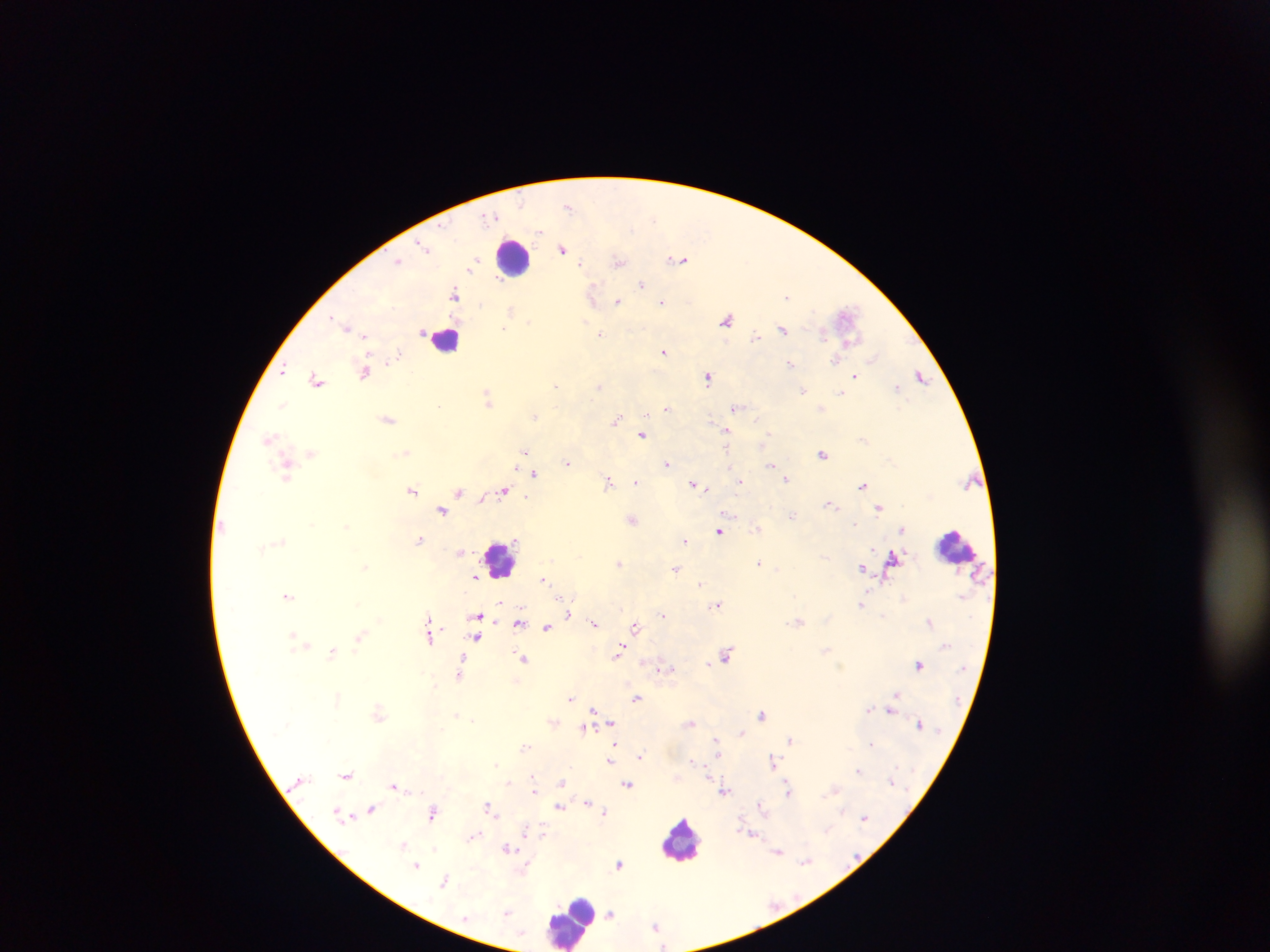 Approximate centers as (x, y) in pixels. Leukocyte locations: (514, 257), (446, 339), (957, 546), (500, 560), (680, 839), (609, 911), (570, 921). Malaria parasite locations: (568, 205), (422, 246), (563, 249), (681, 259), (399, 260), (618, 261), (473, 264), (471, 268), (641, 284), (454, 294), (788, 296), (593, 297), (662, 301), (618, 302), (512, 310), (848, 316), (726, 319), (530, 321), (347, 328), (505, 329), (783, 329), (822, 332), (602, 333), (757, 336), (849, 342), (664, 351), (399, 352), (836, 360), (791, 364), (282, 370), (365, 371), (710, 376), (854, 376), (921, 377), (317, 379), (556, 385), (600, 385), (898, 386), (803, 391), (488, 396), (737, 407), (821, 407), (667, 408), (535, 415), (388, 419), (617, 421), (727, 430), (642, 434), (269, 439), (863, 439), (525, 451), (726, 451), (407, 452), (311, 453), (823, 453), (567, 462), (668, 463), (771, 464), (286, 467), (535, 472), (286, 475), (786, 478), (608, 481), (637, 481), (740, 481), (863, 484), (696, 485), (412, 489), (504, 489), (459, 491), (481, 498), (832, 505), (879, 507), (443, 509), (792, 516), (633, 519), (346, 526), (757, 528), (904, 529), (720, 530), (419, 539), (686, 540), (462, 551), (893, 557), (619, 563), (759, 563), (365, 566), (863, 567), (675, 569), (476, 576), (544, 578), (701, 582), (288, 595), (570, 598), (501, 602), (717, 604), (862, 605), (569, 614), (664, 614), (479, 615), (431, 621), (799, 621), (519, 622), (930, 622), (594, 623), (636, 626), (547, 627), (431, 635), (360, 636), (477, 636), (307, 644), (620, 650), (333, 651), (727, 653), (464, 656), (524, 658), (644, 661), (919, 664), (666, 668), (459, 675), (517, 680), (338, 694), (895, 695), (637, 698), (571, 699), (593, 709), (869, 709), (892, 709), (378, 714), (763, 715), (457, 716), (552, 722), (691, 722), (611, 723), (583, 727), (742, 732), (790, 739), (717, 740), (615, 742), (525, 747), (639, 756), (611, 760), (693, 761), (773, 761), (497, 764), (859, 770), (347, 774), (533, 775), (561, 781), (509, 782), (627, 784), (395, 786), (835, 788), (788, 789), (534, 790), (725, 790), (588, 802), (489, 805), (561, 806), (761, 806), (599, 808), (371, 809), (434, 811), (368, 812), (605, 812), (864, 817), (543, 829), (475, 835), (403, 844), (508, 848), (778, 851), (806, 862), (416, 864), (619, 864), (445, 879), (507, 912), (656, 925), (662, 945). Photographed through a microscope with a mobile-phone camera. Thick blood smear. Sample from Ghana. Image is 1270×952 pixels. Single field of view.